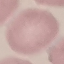
Summary:
  - Malaria status: uninfected
  - Preparation: thin blood smear
  - Capture: smartphone camera at the microscope eyepiece
  - Stain: Giemsa
  - Image type: automatically extracted cell patch, resized to 64 × 64 pixels